Report the malaria status of this cell.
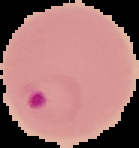
Parasitized.

From a thin blood smear. Image is 139×148 pixels. The area outside the segmented cell region is set to black.